Assess the morphology of the red blood cells.
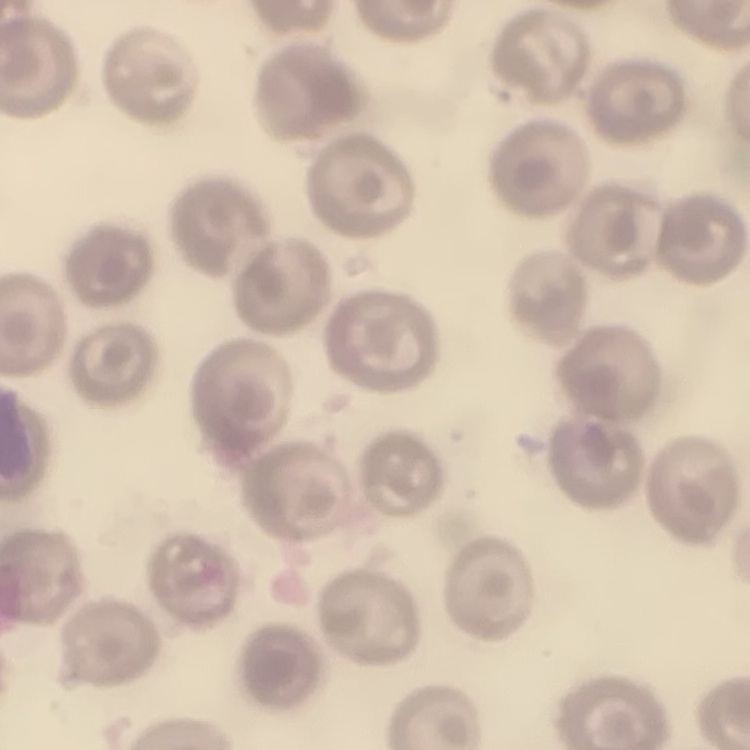
They show no rouleaux formation.

Summary:
  - Stain: Field's or Giemsa
  - Preparation: thin peripheral smear
  - Image type: square crop of a larger photomicrograph